Name the parasite shown.
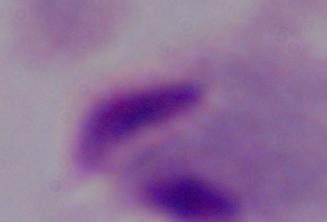

This is a trichomonad.

Summary:
  - Magnification: 1000x
  - Modality: micrograph